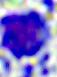

magnification = 400x
identification = leukocyte
modality = micrograph